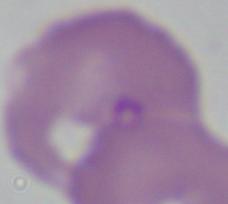

magnification = 1000x
identification = Babesia
modality = micrograph